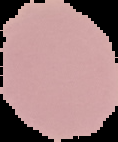
Result: no malaria parasites detected. Image is 118×142 pixels. From a thin blood film. Cell region segmented out of the field of view; the surrounding area is masked to black.